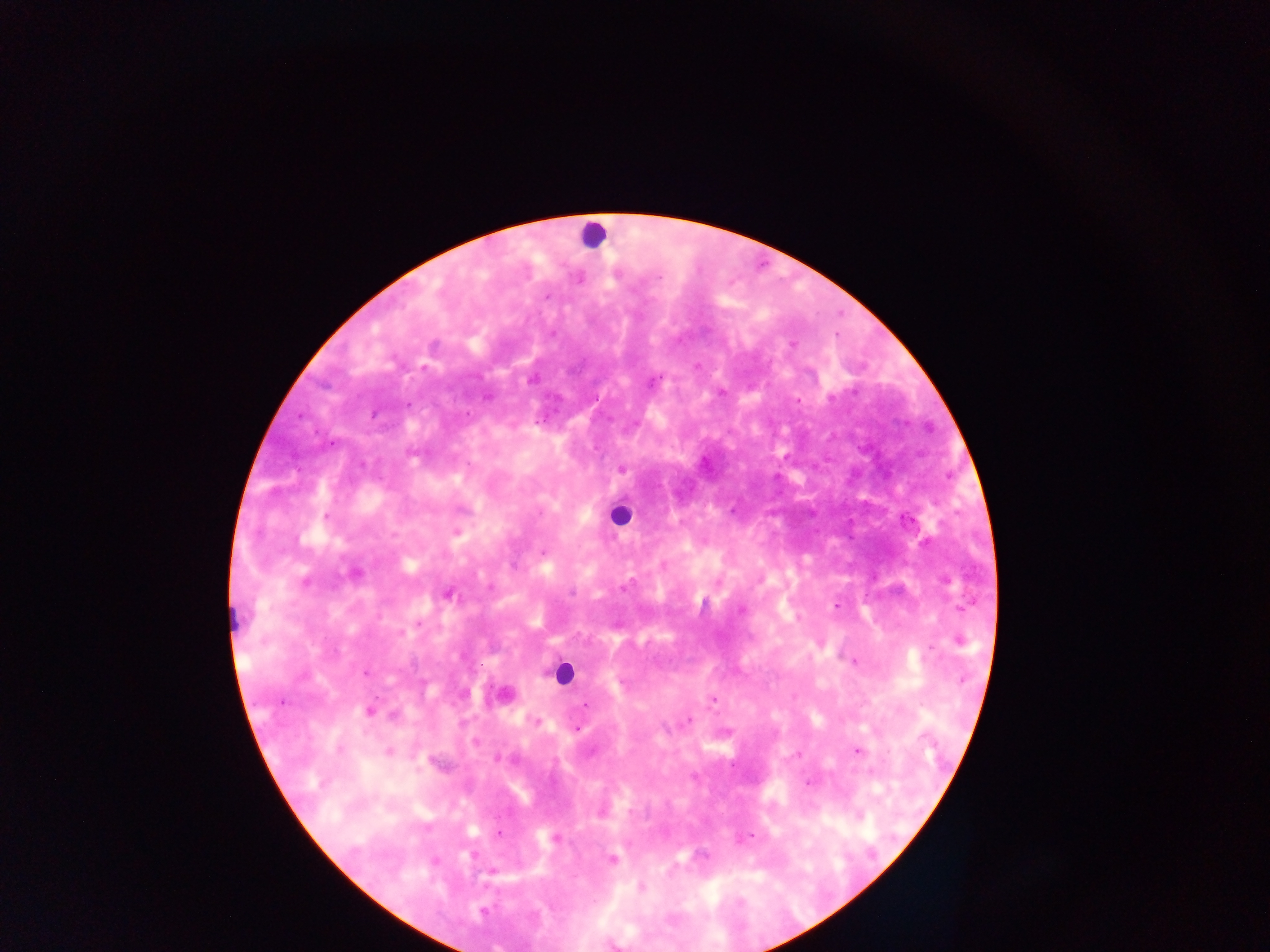

preparation = thick blood smear
leukocyte locations = approximate centers as x y in pixels: 592 234; 620 516; 233 618; 562 672
country = Ghana
capture = mobile-phone photograph through a microscope
field of view = single
Plasmodium parasite locations = approximate centers as x y in pixels: 658 277; 547 297; 553 334; 792 344; 531 380; 652 383; 488 398; 830 398; 407 404; 373 414; 468 414; 301 416; 332 443; 622 469; 326 516; 456 533; 541 552; 663 565; 624 586; 572 592; 449 595; 837 605; 741 611; 419 624; 959 641; 853 661; 365 674; 713 700; 282 702; 587 705; 369 711; 394 715; 689 720; 538 722; 577 729; 339 750; 857 751; 388 752; 796 755; 496 758; 418 769; 809 783; 499 834; 750 836; 555 838; 612 859; 641 887; 483 912
image size = 1270×952 pixels